Classify this cell by malaria status.
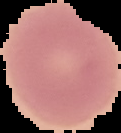

It is uninfected.

image type = segmented cell region on a black background
image size = 121×133 pixels
preparation = thin blood smear